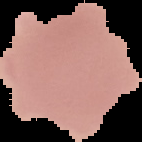 Result: no malaria parasites seen. From a thin blood smear. Cell region segmented out of the field of view; the surrounding area is masked to black. Image is 142×142 pixels.